State which cell type is depicted.
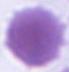
An erythrocyte.

Summary:
  - Modality: photomicrograph
  - Magnification: 1000x